Locate and identify every blood parasite.
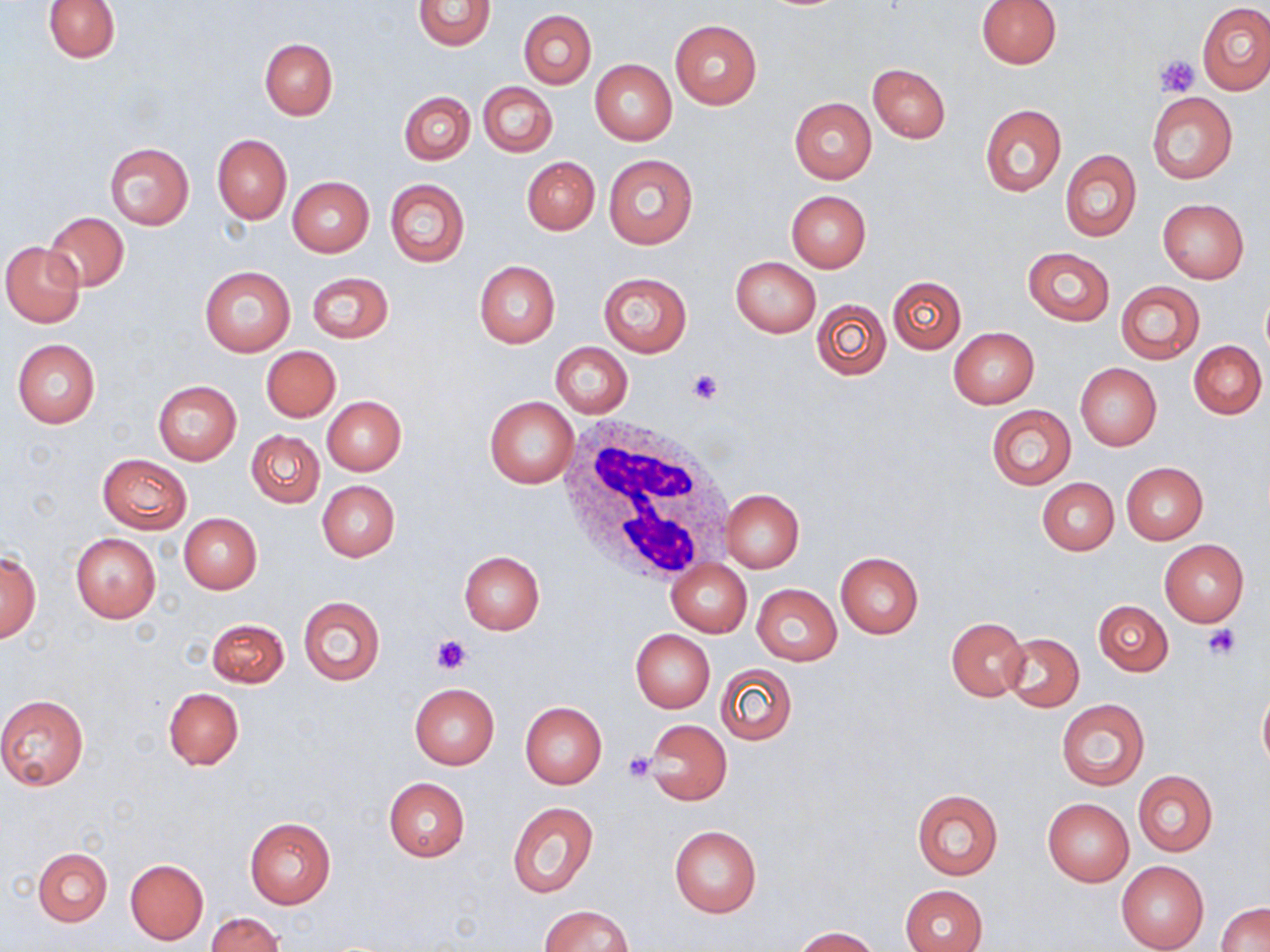
No blood parasites observed.

slide-level diagnosis = no evidence of blood parasites
modality = light microscopy
image size = 1270×952 pixels
field of view = one of a larger specimen
platelet locations = approximate bounding boxes as named x1/y1/x2/y2 corners in pixels: (x1=1154, y1=53, x2=1200, y2=95), (x1=685, y1=368, x2=725, y2=405), (x1=1202, y1=624, x2=1243, y2=661), (x1=431, y1=635, x2=472, y2=675), (x1=623, y1=751, x2=657, y2=781)
magnification = 1000x
uninfected red blood cell locations = approximate bounding boxes as named x1/y1/x2/y2 corners in pixels: (x1=44, y1=0, x2=120, y2=62), (x1=976, y1=0, x2=1061, y2=69), (x1=413, y1=1, x2=495, y2=51), (x1=1198, y1=2, x2=1270, y2=95), (x1=519, y1=10, x2=596, y2=88), (x1=670, y1=20, x2=761, y2=108), (x1=260, y1=37, x2=338, y2=120), (x1=590, y1=60, x2=676, y2=145), (x1=867, y1=63, x2=951, y2=143), (x1=478, y1=82, x2=557, y2=157), (x1=400, y1=91, x2=475, y2=164), (x1=1147, y1=92, x2=1238, y2=185), (x1=789, y1=98, x2=876, y2=184), (x1=979, y1=103, x2=1066, y2=196), (x1=212, y1=134, x2=291, y2=223), (x1=103, y1=142, x2=194, y2=229), (x1=1059, y1=150, x2=1140, y2=242), (x1=602, y1=154, x2=698, y2=250), (x1=521, y1=156, x2=599, y2=234), (x1=287, y1=177, x2=373, y2=257), (x1=384, y1=179, x2=470, y2=266), (x1=786, y1=190, x2=871, y2=273), (x1=1158, y1=199, x2=1248, y2=283), (x1=42, y1=211, x2=129, y2=292), (x1=2, y1=241, x2=85, y2=327), (x1=1022, y1=247, x2=1113, y2=326), (x1=731, y1=256, x2=821, y2=337), (x1=475, y1=261, x2=559, y2=348), (x1=199, y1=265, x2=296, y2=357), (x1=307, y1=272, x2=393, y2=343), (x1=598, y1=272, x2=692, y2=356), (x1=887, y1=276, x2=965, y2=354), (x1=1115, y1=281, x2=1205, y2=365), (x1=1261, y1=291, x2=1270, y2=363), (x1=811, y1=298, x2=892, y2=380), (x1=948, y1=328, x2=1040, y2=409), (x1=12, y1=338, x2=101, y2=430), (x1=1189, y1=341, x2=1267, y2=419), (x1=551, y1=342, x2=633, y2=417), (x1=261, y1=346, x2=341, y2=421), (x1=1075, y1=363, x2=1161, y2=451), (x1=152, y1=379, x2=242, y2=465), (x1=322, y1=396, x2=406, y2=475), (x1=485, y1=397, x2=579, y2=488), (x1=987, y1=405, x2=1076, y2=488), (x1=247, y1=430, x2=324, y2=506), (x1=98, y1=454, x2=191, y2=533), (x1=1120, y1=461, x2=1208, y2=545), (x1=1037, y1=477, x2=1119, y2=555), (x1=316, y1=480, x2=400, y2=562), (x1=720, y1=490, x2=804, y2=572), (x1=179, y1=513, x2=262, y2=593), (x1=70, y1=532, x2=160, y2=623), (x1=1159, y1=540, x2=1248, y2=626), (x1=459, y1=551, x2=544, y2=634), (x1=834, y1=551, x2=924, y2=638), (x1=1, y1=552, x2=41, y2=642), (x1=666, y1=561, x2=751, y2=636), (x1=752, y1=584, x2=842, y2=666), (x1=297, y1=595, x2=385, y2=686), (x1=1094, y1=600, x2=1173, y2=675), (x1=947, y1=617, x2=1029, y2=701), (x1=206, y1=618, x2=289, y2=688), (x1=630, y1=629, x2=715, y2=712), (x1=1002, y1=632, x2=1084, y2=710), (x1=716, y1=663, x2=798, y2=745), (x1=409, y1=683, x2=499, y2=769), (x1=1258, y1=684, x2=1270, y2=776), (x1=163, y1=688, x2=243, y2=769), (x1=0, y1=693, x2=89, y2=790), (x1=1056, y1=699, x2=1150, y2=790), (x1=519, y1=702, x2=607, y2=790), (x1=644, y1=719, x2=731, y2=805), (x1=1132, y1=771, x2=1218, y2=857), (x1=382, y1=777, x2=470, y2=861), (x1=911, y1=788, x2=1003, y2=880), (x1=1042, y1=798, x2=1134, y2=887), (x1=507, y1=802, x2=597, y2=898), (x1=244, y1=815, x2=336, y2=909), (x1=669, y1=825, x2=762, y2=917), (x1=33, y1=848, x2=111, y2=926), (x1=124, y1=858, x2=208, y2=945), (x1=1117, y1=861, x2=1208, y2=951), (x1=898, y1=884, x2=986, y2=952), (x1=1215, y1=903, x2=1270, y2=952), (x1=539, y1=904, x2=633, y2=952), (x1=206, y1=912, x2=284, y2=951), (x1=791, y1=926, x2=881, y2=951)
preparation = thin blood film
white blood cell locations = approximate bounding boxes as named x1/y1/x2/y2 corners in pixels: (x1=557, y1=415, x2=734, y2=583)
stain = May-Grünwald-Giemsa